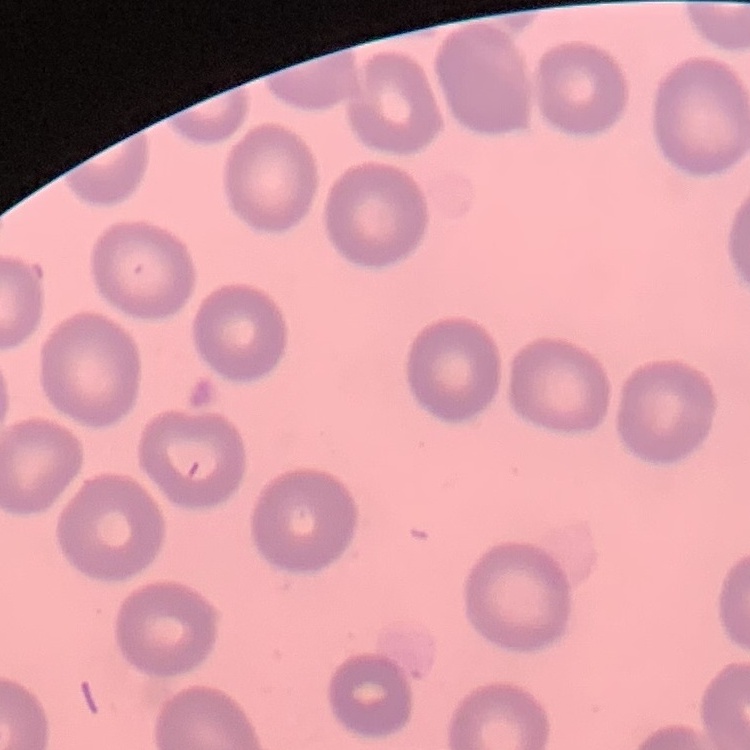

erythrocyte_morphology: no rouleaux formation
stain: Field's or Giemsa
image_type: square crop of a larger photomicrograph
preparation: thin blood smear